State the blood parasite species.
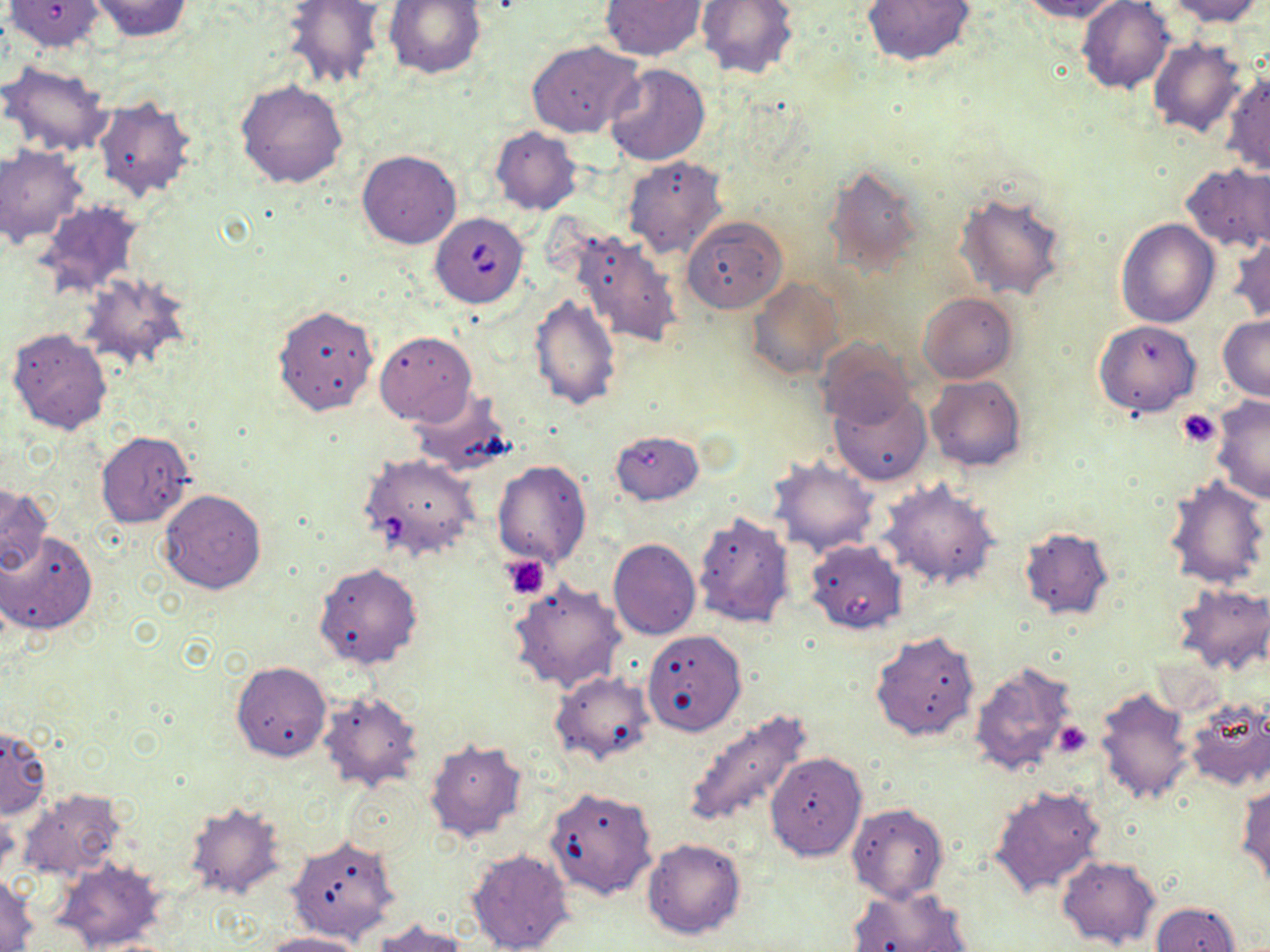

Babesia divergens.

Summary:
  - Coordinate format: approximate bounding boxes as (x1,y1)-(x2,y2) corner pairs in pixels
  - Uninfected red blood cell locations: (85,0)-(197,41), (384,0)-(486,78), (600,0)-(707,61), (696,0)-(801,80), (862,0)-(977,68), (1020,0)-(1127,22), (1076,0)-(1174,93), (1163,0)-(1263,25), (6,1)-(105,51), (280,1)-(387,91), (1148,38)-(1247,138), (527,41)-(643,139), (0,59)-(115,157), (606,64)-(710,166), (1223,71)-(1270,175), (236,78)-(349,189), (93,97)-(198,202), (490,128)-(582,215), (0,146)-(87,246), (356,150)-(461,250), (622,156)-(728,260), (1181,162)-(1270,253), (824,164)-(924,273), (955,188)-(1068,301), (34,201)-(145,298), (681,215)-(788,314), (1116,219)-(1220,328), (565,229)-(684,348), (1228,233)-(1270,325), (80,273)-(191,374), (748,276)-(844,381), (917,292)-(1017,383), (529,293)-(622,411), (272,304)-(379,415), (1218,315)-(1270,402), (1094,320)-(1200,418), (6,327)-(112,435), (375,331)-(477,425), (817,339)-(916,431), (926,375)-(1025,471), (829,387)-(933,487), (408,388)-(513,475), (1210,396)-(1270,504), (610,429)-(703,505), (96,430)-(193,528), (767,455)-(880,558), (493,458)-(592,570), (1163,475)-(1269,590), (878,478)-(1001,589), (0,485)-(52,576), (159,489)-(266,595), (691,512)-(796,629), (1017,525)-(1114,619), (0,531)-(97,634), (608,538)-(700,641), (804,539)-(908,635), (314,561)-(424,670), (509,577)-(626,694), (1171,583)-(1270,676), (642,629)-(746,737), (870,629)-(980,742), (232,660)-(331,761), (968,660)-(1080,780), (550,670)-(655,767), (1093,685)-(1195,806), (317,688)-(424,792), (1182,697)-(1270,792), (681,710)-(813,830), (1050,716)-(1095,764), (1,725)-(51,819), (424,738)-(528,843), (764,752)-(868,859), (343,779)-(428,861), (988,784)-(1105,898), (1237,784)-(1270,891), (544,786)-(658,901), (17,788)-(125,883), (182,801)-(286,900), (847,803)-(948,903), (286,834)-(401,944), (642,838)-(745,940), (466,847)-(574,952), (1056,855)-(1160,949), (55,859)-(167,950), (1,874)-(38,951), (846,884)-(973,952), (1152,902)-(1240,952), (369,919)-(471,951), (257,931)-(369,952)
  - Babesia divergens-infected red blood cell locations: (430,212)-(529,309), (366,459)-(489,561)
  - Platelet locations: (1177,408)-(1221,448), (503,555)-(550,599), (1053,722)-(1091,757)
  - Image size: 1270×952 pixels
  - Preparation: thin blood film
  - Modality: light microscopy
  - Magnification: 1000x
  - Stain: May-Grünwald-Giemsa
  - Field of view: one of a larger specimen